Describe the morphology of the erythrocytes.
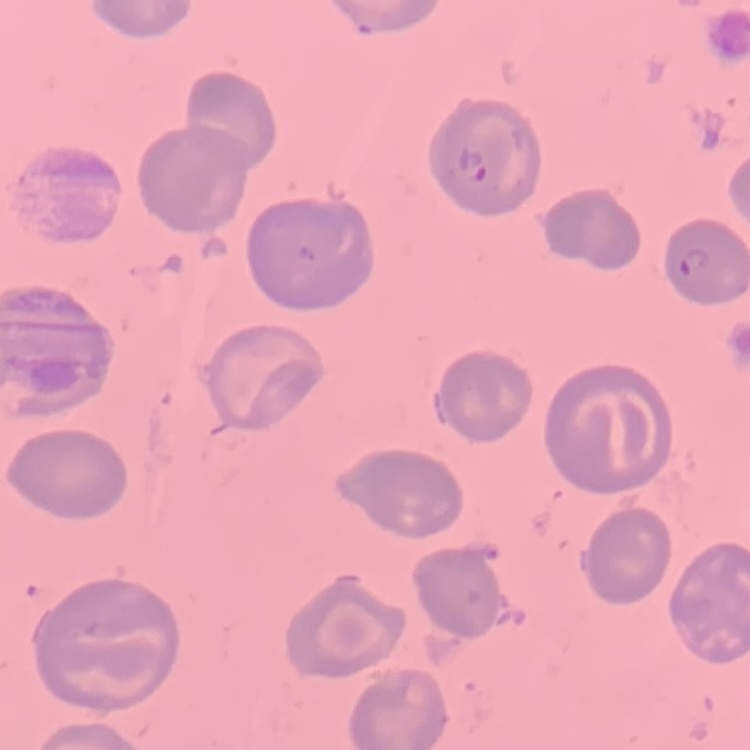

They show no rouleaux formation.

Thin peripheral smear. Stained with either Field's or Giemsa. One tile cut from a larger photomicrograph.